Identify the parasite.
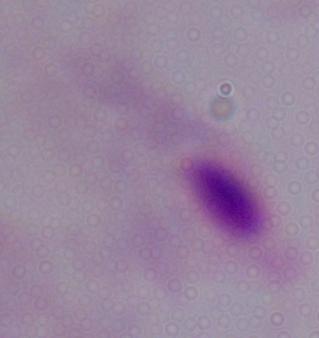
This is a trichomonad.

Summary:
  - Modality: photomicrograph
  - Magnification: 1000x